State which parasite is depicted.
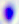
Toxoplasma gondii.

{
  "magnification": "400x",
  "modality": "photomicrograph"
}